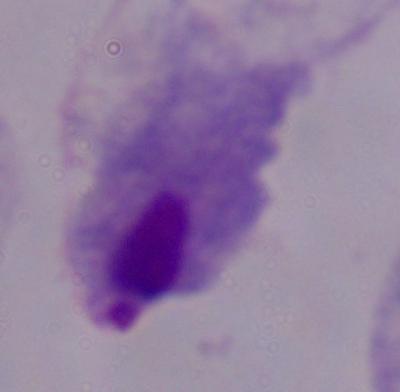
Summary:
  - Modality: photomicrograph
  - Magnification: 1000x
  - Identification: trichomonad